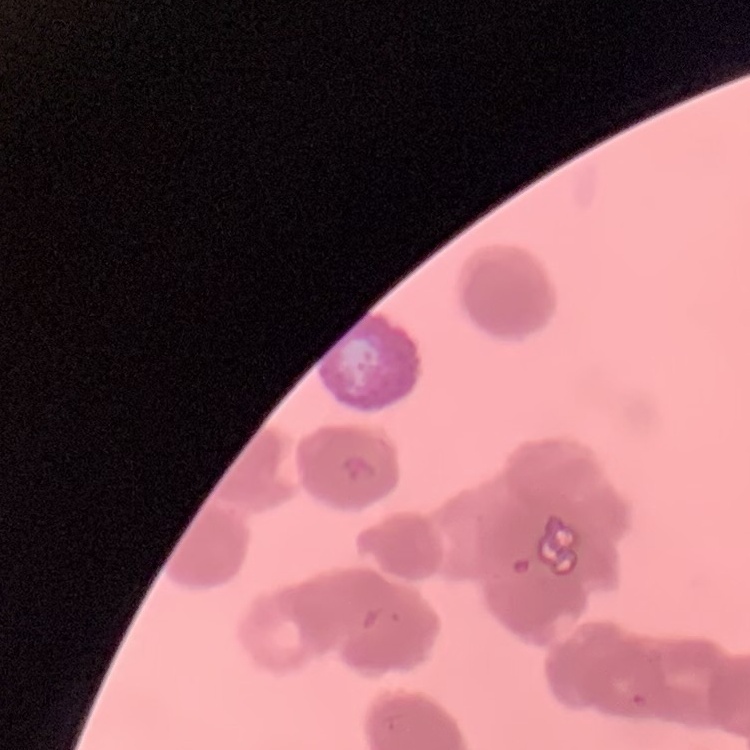
The erythrocytes exhibit rouleaux formation. Stained with either Field's or Giemsa. One tile cut from a larger photomicrograph. Thin blood smear.